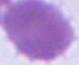

Summary:
  - Modality: photomicrograph
  - Magnification: 1000x
  - Identification: erythrocyte